Mark where cells are.
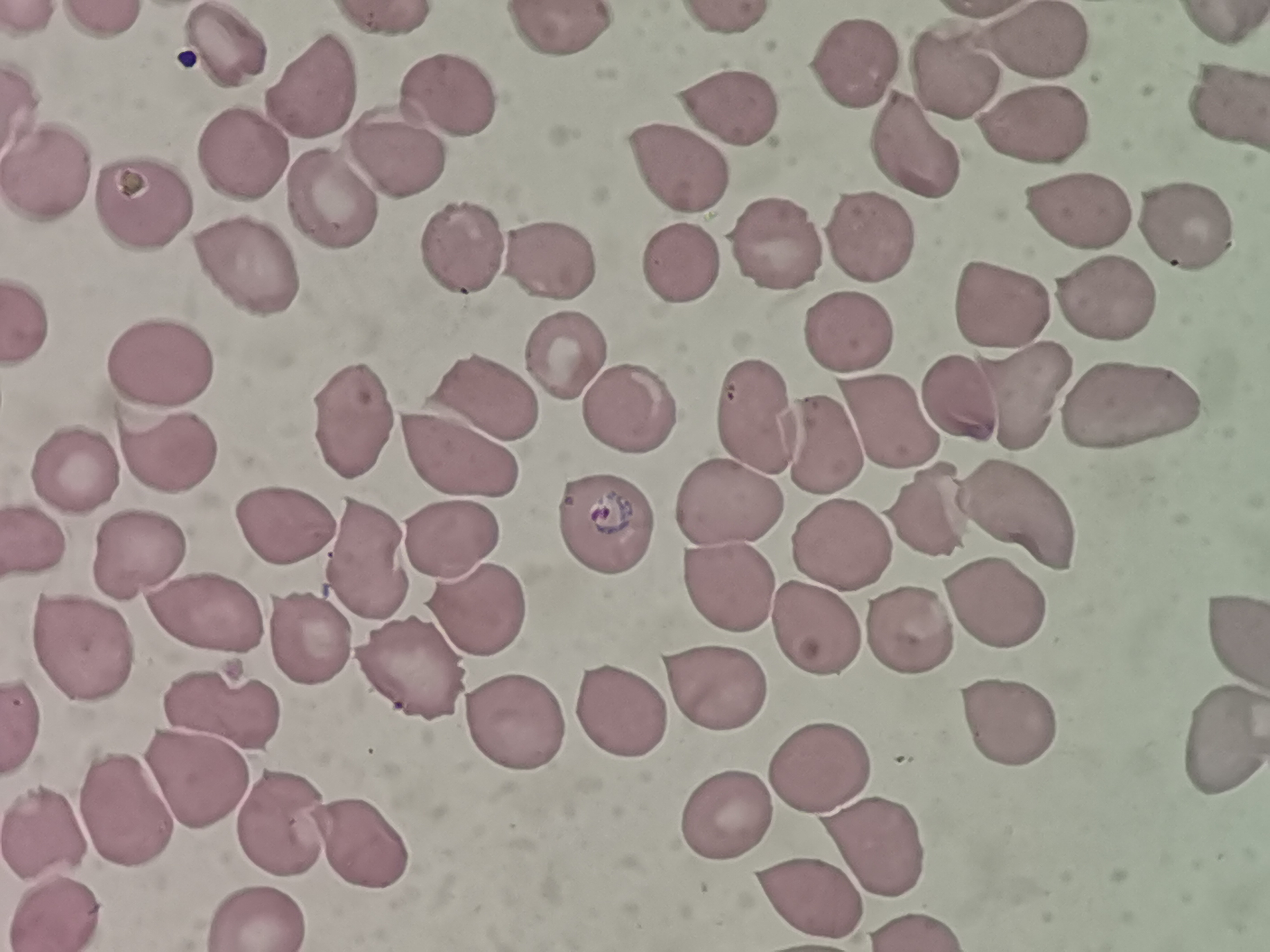

Approximate centers as {x, y} in pixels.
Cells: {560, 32}, {223, 42}, {1039, 43}, {855, 64}, {945, 72}, {316, 88}, {446, 99}, {1223, 103}, {727, 110}, {1035, 120}, {913, 153}, {240, 154}, {392, 159}, {678, 168}, {51, 174}, {329, 204}, {147, 205}, {1077, 214}, {1177, 228}, {868, 231}, {785, 250}, {557, 256}, {458, 261}, {679, 264}, {250, 274}, {1106, 297}, {996, 311}, {29, 322}, {849, 334}, {564, 350}, {155, 366}, {485, 395}, {1017, 395}, {963, 396}, {1129, 401}, {760, 409}, {625, 412}, {885, 416}, {347, 421}, {818, 448}, {461, 457}, {158, 458}, {74, 474}, {734, 506}, {931, 510}, {1021, 520}, {601, 523}, {284, 525}, {37, 538}, {458, 538}, {839, 539}, {146, 559}, {375, 563}, {729, 594}, {994, 603}, {486, 614}, {208, 615}, {907, 628}, {816, 630}, {1226, 632}, {312, 643}, {82, 644}, {410, 677}, {713, 688}, {613, 703}, {220, 705}, {1007, 722}, {519, 734}, {1225, 735}, {812, 765}, {187, 775}, {124, 801}, {728, 816}, {287, 824}, {51, 828}, {359, 841}, {861, 842}, {801, 894}, {64, 909}, {261, 910}.

Photographed with a smartphone camera at the microscope eyepiece. One field from this slide. Thin blood smear. Giemsa stain. Image is 1270×952 pixels.